Give the position of every leukocyte visible.
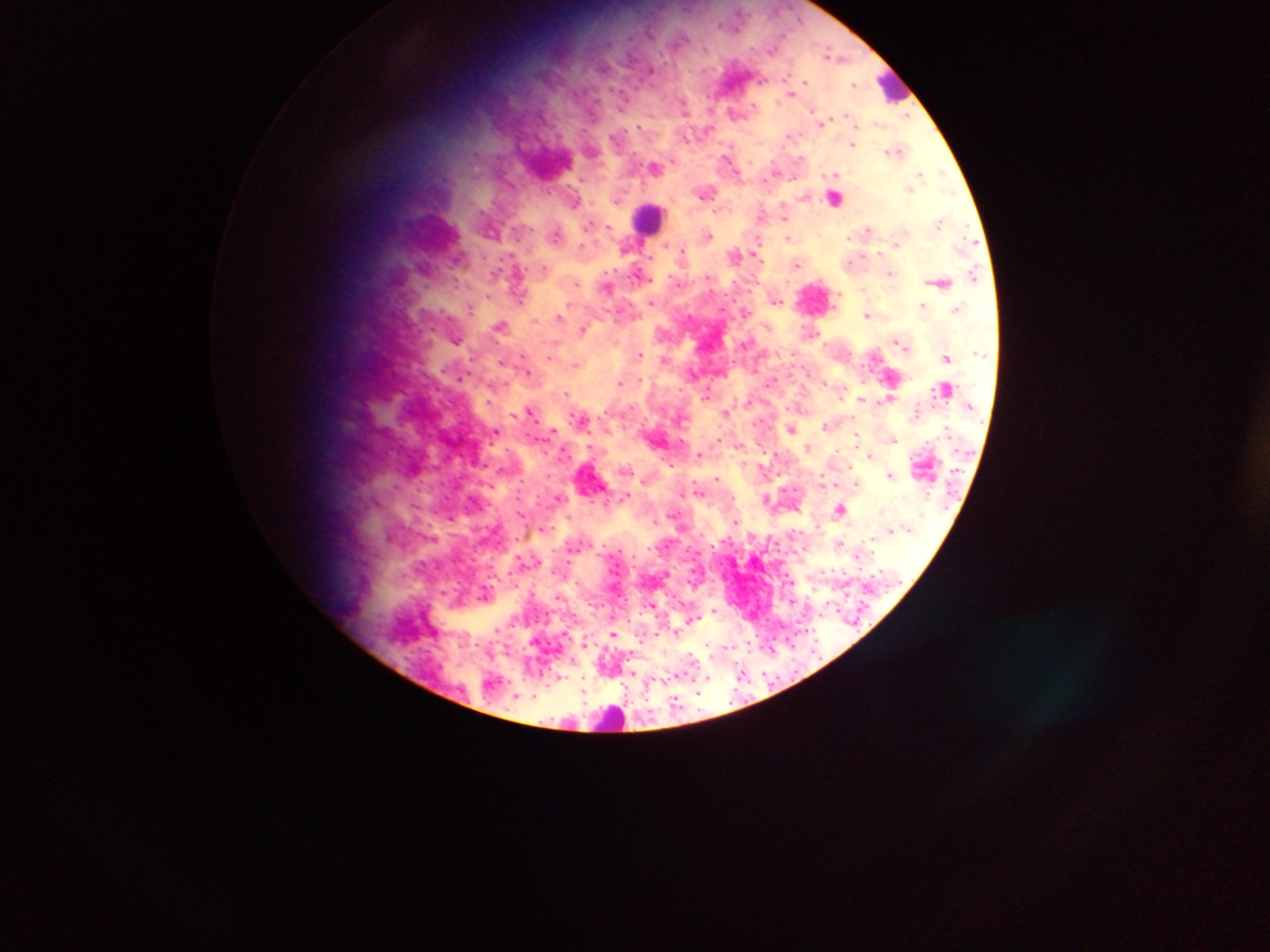
Approximate centers as x y in pixels.
Leukocytes: 892 92; 647 223.

Summary:
  - Plasmodium parasite locations: 829 55; 834 58; 803 82; 856 83; 752 105; 820 124; 788 136; 853 145; 895 150; 918 173; 791 178; 704 198; 586 224; 869 231; 710 234; 788 238; 961 238; 757 245; 682 252; 797 264; 850 264; 546 267; 610 272; 891 272; 706 276; 652 281; 838 293; 775 301; 833 306; 560 315; 746 315; 867 315; 581 329; 897 338; 455 342; 901 342; 639 354; 664 357; 575 365; 528 372; 753 372; 622 382; 566 393; 705 398; 485 402; 530 410; 726 412; 581 418; 756 424; 823 426; 791 429; 894 439; 738 447; 700 453; 764 453; 869 455; 666 460; 853 468; 548 473; 890 473; 719 478; 701 493; 626 496; 377 503; 839 508; 675 510; 568 516; 519 517; 654 522; 873 540; 581 541; 841 541; 862 541; 591 545; 666 545; 712 547; 649 549; 553 551; 578 551; 620 551; 858 557; 568 562; 617 565; 823 571; 833 571; 844 573; 618 574; 565 576; 688 580; 576 583; 557 598; 681 603; 712 611; 640 613; 656 616; 699 618; 629 621; 689 622; 675 632; 657 634; 613 635; 756 636; 775 637; 786 638; 641 642; 586 643; 746 643; 707 644; 793 645; 725 648; 763 648; 692 653; 748 653; 711 656; 572 660; 628 660; 700 660; 633 671; 796 672; 685 673; 763 673; 675 676; 582 678; 778 678; 740 679; 794 681; 621 682; 750 682; 547 685; 627 688; 734 689; 584 691; 698 692; 533 696; 677 697; 646 700; 729 702; 746 702; 585 704; 625 705; 698 708; 650 711; 584 716; 553 720; 539 722
  - Country: Ghana
  - Preparation: thick blood smear
  - Field of view: single
  - Image size: 1270×952 pixels
  - Capture: mobile-phone photograph through a microscope